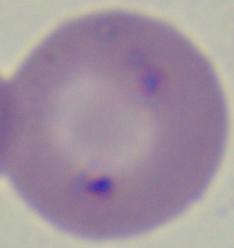 A Babesia parasite is shown. Micrograph. Captured at 1000x magnification.